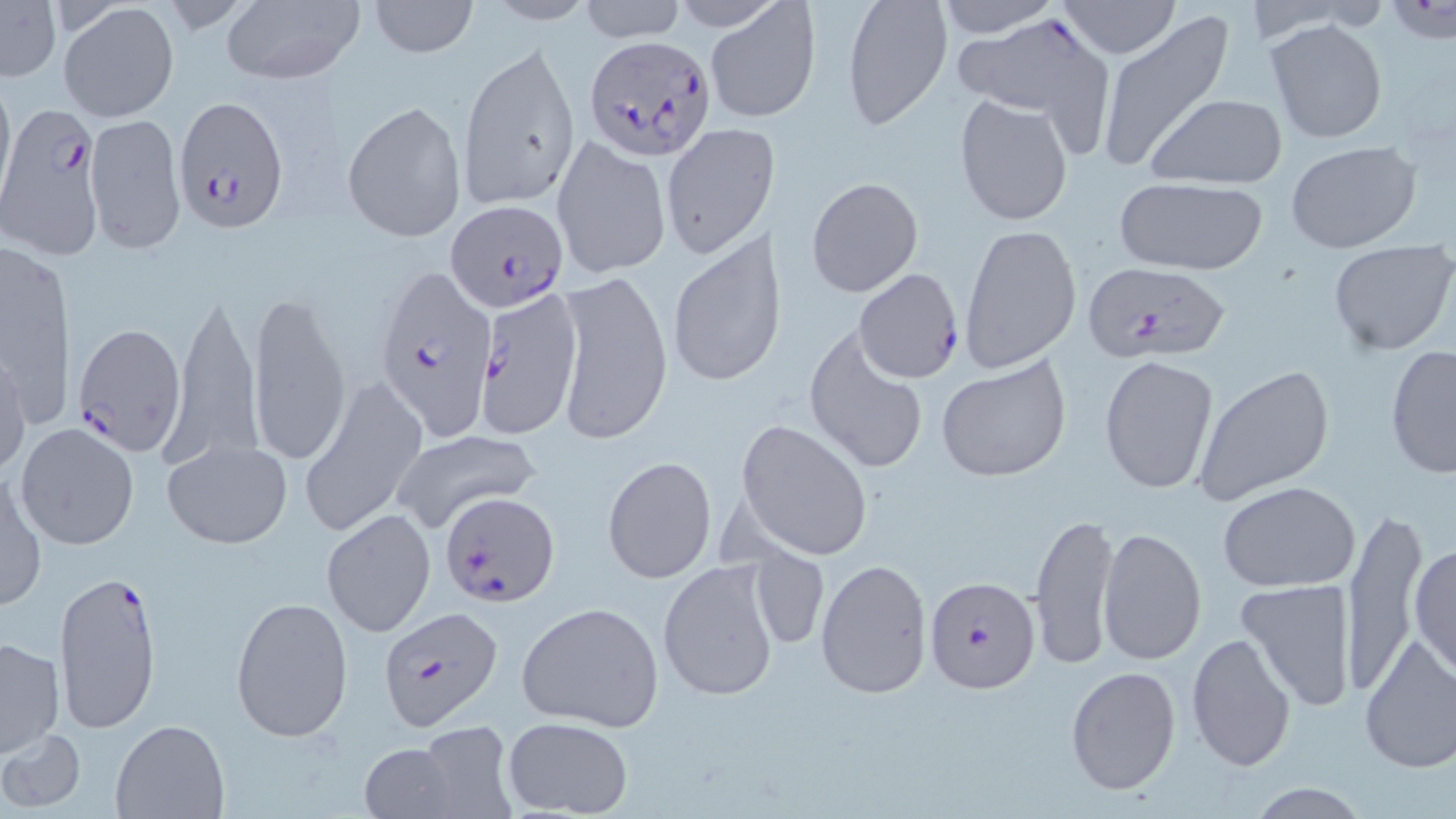

Approximate bounding boxes as (x1, y1, x2, y2) in pixels. Uninfected red blood cell locations: (217, 0, 367, 85), (367, 0, 478, 57), (578, 0, 688, 43), (841, 0, 951, 131), (934, 0, 1060, 38), (1057, 0, 1182, 59), (479, 1, 599, 26), (0, 2, 60, 84), (59, 2, 179, 122), (704, 3, 820, 123), (955, 11, 1114, 139), (1096, 12, 1237, 175), (1265, 18, 1388, 144), (460, 41, 583, 214), (0, 72, 16, 205), (954, 94, 1074, 227), (1147, 95, 1286, 188), (342, 99, 467, 242), (86, 111, 187, 253), (660, 122, 776, 259), (551, 135, 671, 281), (1284, 138, 1423, 254), (805, 175, 925, 299), (1114, 177, 1269, 274), (958, 224, 1084, 373), (667, 233, 782, 390), (0, 238, 74, 429), (1327, 240, 1456, 356), (554, 270, 673, 445), (163, 286, 262, 472), (248, 291, 352, 466), (803, 326, 930, 475), (0, 345, 30, 477), (1383, 347, 1456, 478), (937, 354, 1071, 483), (1099, 354, 1219, 493), (1193, 364, 1335, 506), (299, 373, 429, 537), (735, 419, 874, 561), (16, 422, 140, 550), (390, 430, 542, 537), (160, 435, 294, 550), (602, 456, 718, 582), (1, 467, 47, 613), (1217, 481, 1360, 593), (1337, 500, 1429, 698), (322, 509, 437, 638), (1029, 509, 1120, 670), (1098, 527, 1206, 665), (1409, 537, 1455, 681), (749, 546, 830, 653), (815, 555, 932, 699), (658, 558, 783, 703), (1236, 579, 1358, 711), (229, 596, 352, 741), (516, 600, 665, 733), (1187, 632, 1298, 773), (1358, 633, 1456, 773), (1, 635, 65, 757), (1065, 665, 1181, 798), (502, 716, 635, 817), (110, 719, 230, 817), (412, 724, 519, 818), (1, 726, 86, 812), (357, 740, 467, 818), (1239, 781, 1376, 817). Plasmodium falciparum-infected red blood cell locations: (583, 34, 716, 160), (171, 94, 289, 229), (1, 103, 105, 261), (447, 199, 570, 314), (373, 261, 499, 440), (1079, 261, 1232, 366), (852, 267, 965, 384), (474, 289, 582, 442), (73, 321, 186, 457), (433, 489, 558, 604), (52, 568, 166, 741), (925, 575, 1041, 693), (380, 607, 504, 731). Slide-level diagnosis: Plasmodium falciparum. 1000x magnification. May-Grünwald-Giemsa stain. Image is 1456×819 pixels. One field of a larger specimen. Thin blood smear. Light microscopy.